Identify the parasite.
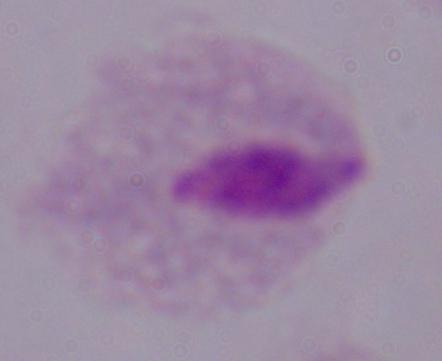

This is a trichomonad.

{
  "magnification": "1000x",
  "modality": "photomicrograph"
}